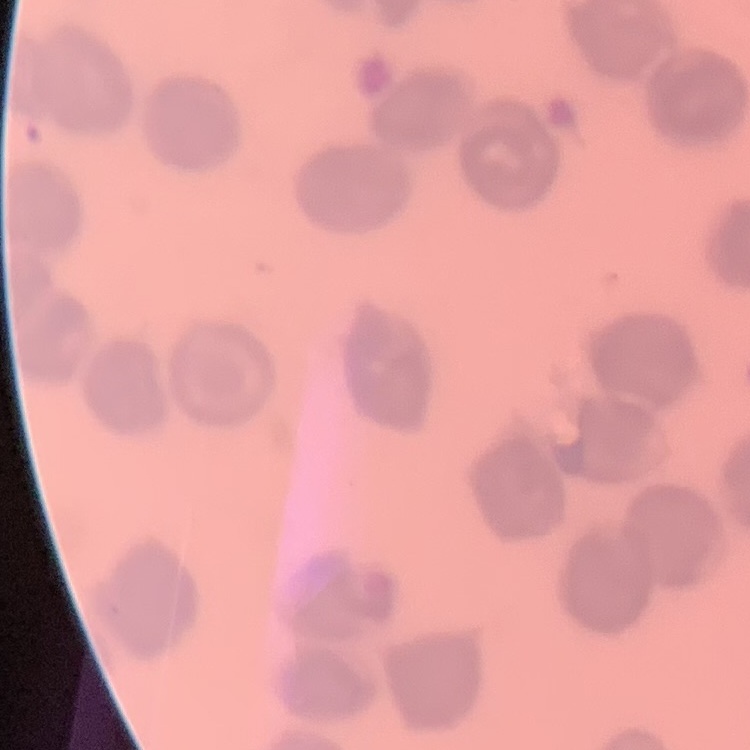

The erythrocytes exhibit no rouleaux formation. Thin blood smear. Square crop of a larger photomicrograph. Field's or Giemsa stain.